State which parasite is depicted.
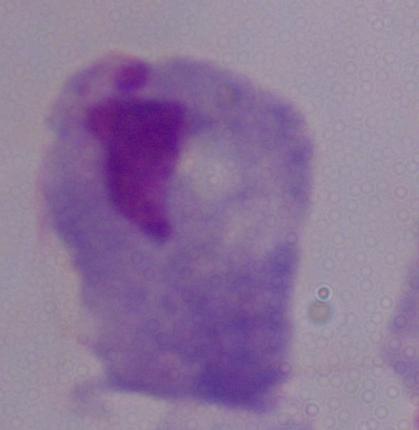

A trichomonad.

Summary:
  - Modality: photomicrograph
  - Magnification: 1000x